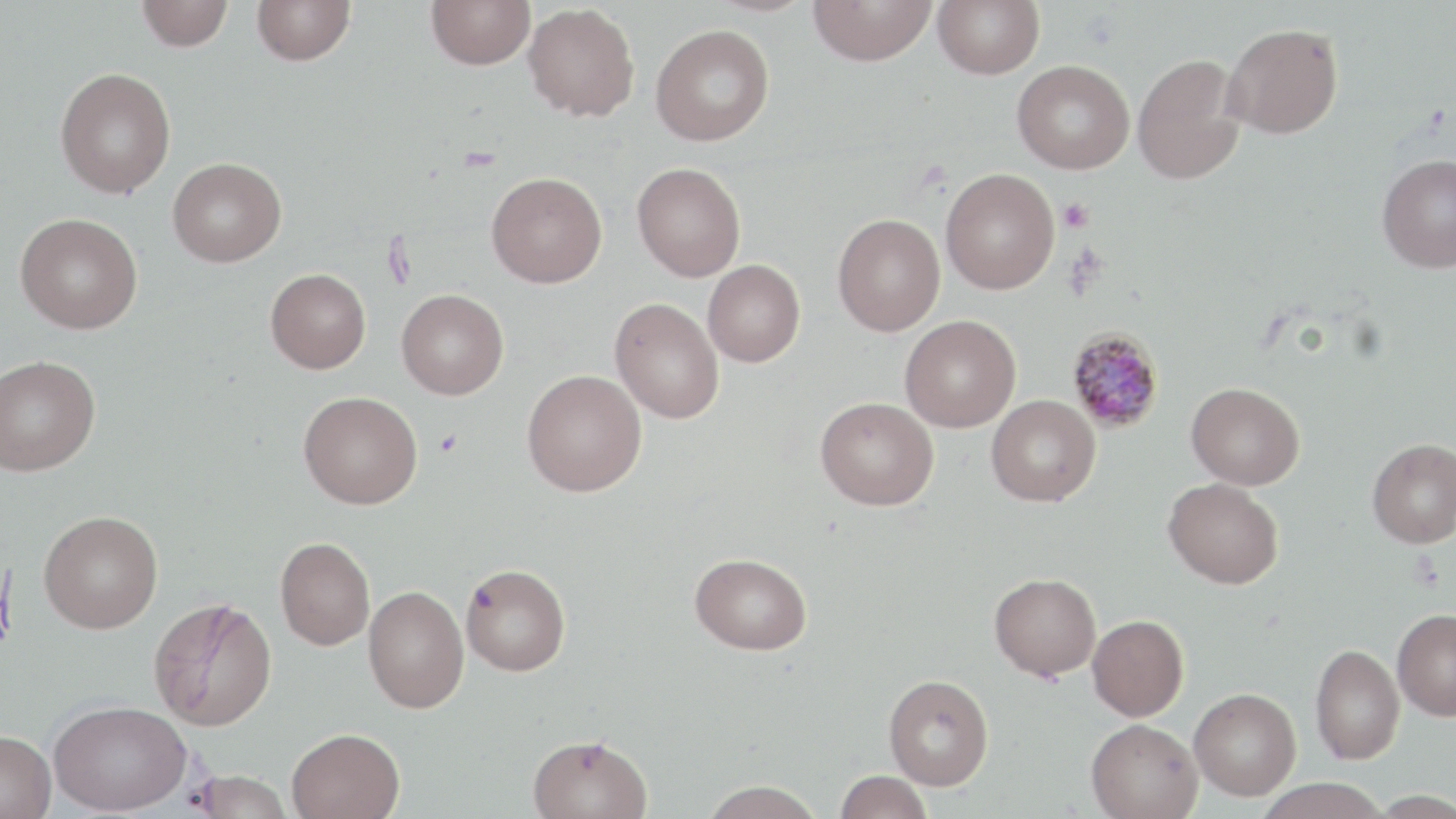

Approximate bounding boxes as (x1, y1, x2, y2) in pixels. Plasmodium malariae-infected red blood cell locations: (1066, 327, 1165, 433). Uninfected red blood cell locations: (136, 0, 234, 51), (252, 0, 355, 65), (426, 0, 535, 70), (808, 0, 936, 66), (933, 0, 1045, 80), (523, 3, 640, 122), (1222, 22, 1343, 139), (650, 24, 775, 146), (1132, 53, 1246, 185), (1012, 60, 1135, 174), (55, 67, 176, 198), (1377, 153, 1456, 272), (167, 157, 286, 266), (631, 162, 746, 281), (940, 167, 1060, 294), (486, 171, 607, 288), (15, 212, 143, 333), (832, 213, 945, 336), (703, 260, 805, 367), (265, 268, 371, 373), (396, 289, 508, 399), (610, 297, 724, 423), (900, 315, 1020, 432), (0, 354, 100, 476), (522, 370, 646, 496), (1187, 382, 1304, 489), (298, 391, 422, 509), (986, 395, 1100, 506), (815, 397, 938, 510), (1367, 439, 1456, 548), (1163, 478, 1283, 589), (38, 511, 163, 633), (275, 536, 375, 650), (690, 553, 811, 654), (461, 562, 571, 675), (990, 572, 1101, 680), (363, 586, 469, 713), (149, 597, 277, 731), (1393, 609, 1456, 720), (1087, 614, 1189, 720), (1310, 643, 1404, 764), (884, 674, 994, 789), (1189, 687, 1301, 800), (48, 700, 191, 815), (1086, 718, 1203, 819), (287, 728, 405, 819), (0, 731, 56, 819), (527, 733, 653, 819), (835, 770, 932, 818), (186, 771, 294, 818), (1253, 778, 1390, 819), (700, 780, 825, 819). Platelet locations: (1058, 197, 1094, 232), (434, 428, 462, 458). Slide-level diagnosis: Plasmodium malariae. May-Grünwald-Giemsa-stained preparation. Captured at 1000x magnification. Image is 1456×819 pixels. Single field of view. Thin blood film. Light microscopy.